Classify this cell by malaria status.
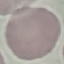
Uninfected.

capture: smartphone camera at the microscope eyepiece
image_type: automatically extracted cell patch, resized to 64 × 64 pixels
preparation: thin smear
stain: Giemsa